Point out each malaria parasite.
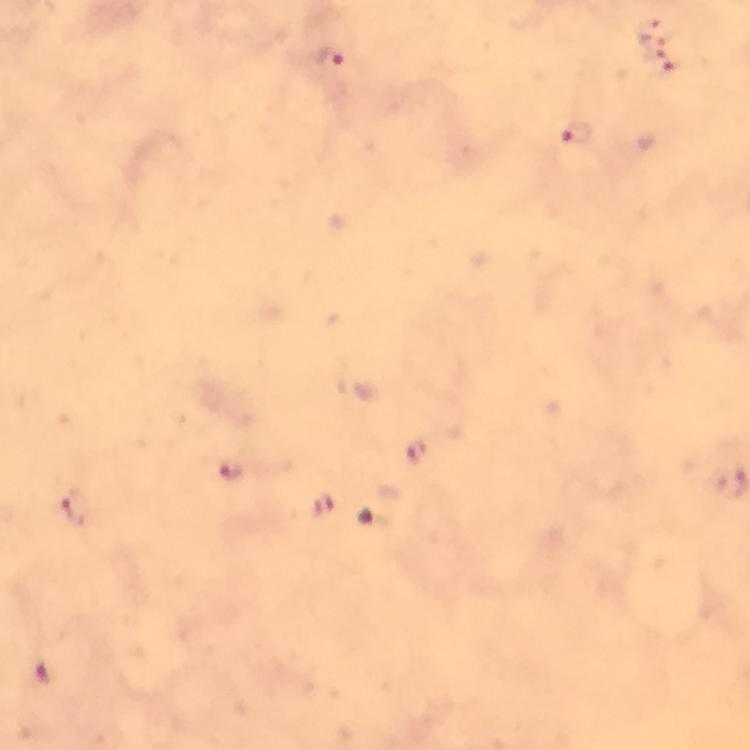

Approximate object centers, in pixels from the top-left corner.
Malaria parasites: (x=651, y=31), (x=327, y=58), (x=660, y=61), (x=577, y=136), (x=415, y=450), (x=230, y=470), (x=323, y=505), (x=73, y=511), (x=42, y=673).

Summary:
  - Preparation: thick blood smear
  - Context: from a diagnostic examination for malaria
  - Immersion oil: used
  - Stain: Giemsa
  - Image size: 750×750 pixels
  - Capture: smartphone camera through the microscope
  - Cropped from: a single field of view
  - Magnification: 100x